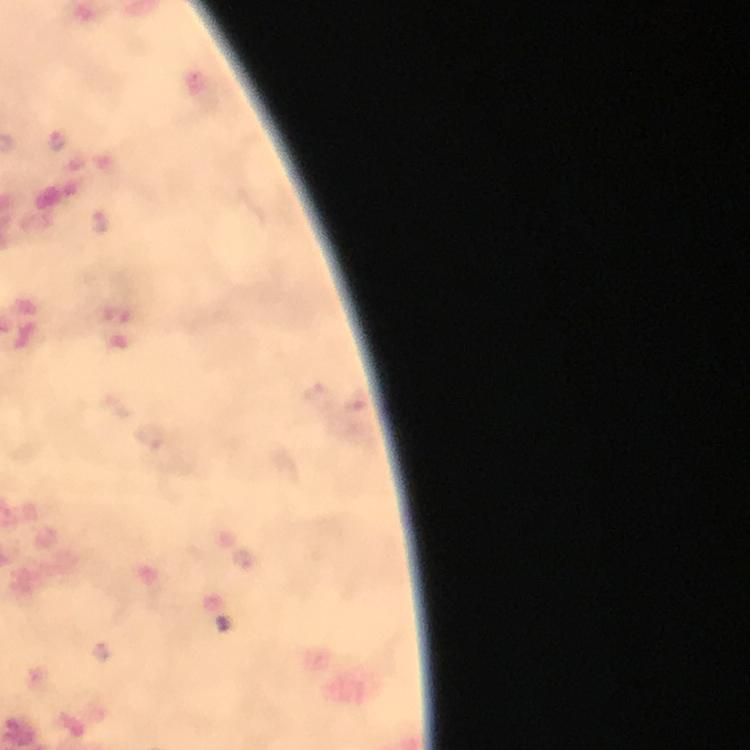

magnification = 100x
stain = Giemsa
Plasmodium parasite locations = approximate centers as [x, y] in pixels: [57, 140], [321, 396], [151, 437]
capture = smartphone photograph through a microscope
context = from a diagnostic examination for malaria
preparation = thick blood film
image size = 750×750 pixels
cropped from = a single field of view
immersion oil = applied